Describe the morphology of the erythrocytes.
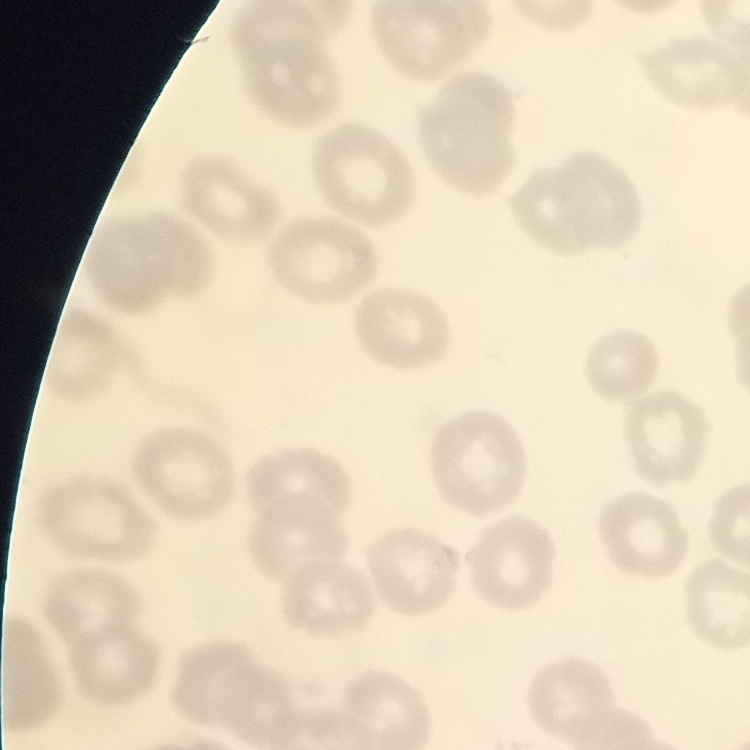
They show no rouleaux formation.

Summary:
  - Stain: Field's or Giemsa
  - Image type: square crop of a larger photomicrograph
  - Preparation: thin blood smear